Point out each leukocyte.
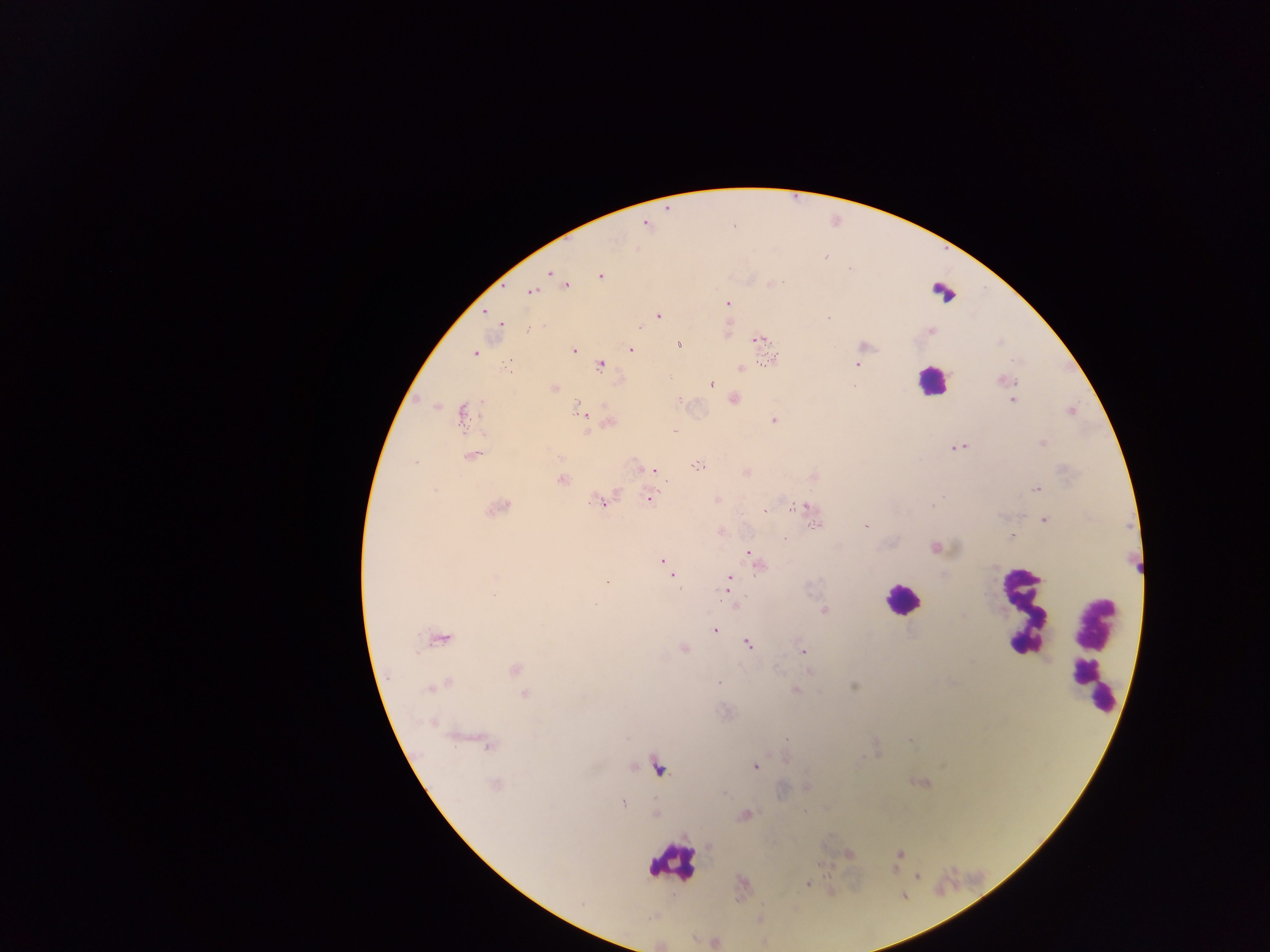

Approximate centers as [x, y] in pixels.
Leukocytes: [943, 293], [932, 380], [901, 598], [1024, 612], [1097, 652], [672, 861].

field of view = single
country = Ghana
image size = 1270×952 pixels
capture = mobile-phone photograph through a microscope
malaria parasite locations = approximate centers as [x, y] in pixels: [666, 209], [646, 225], [551, 272], [600, 276], [771, 284], [566, 285], [532, 291], [728, 303], [484, 311], [658, 316], [500, 324], [639, 328], [931, 330], [757, 340], [679, 343], [864, 345], [630, 349], [574, 351], [474, 353], [772, 359], [509, 360], [600, 364], [856, 364], [740, 368], [1003, 380], [710, 383], [554, 388], [733, 398], [1012, 400], [578, 404], [435, 406], [1070, 410], [581, 412], [462, 413], [773, 420], [609, 422], [587, 430], [674, 431], [1043, 442], [959, 446], [470, 455], [696, 465], [654, 469], [745, 471], [813, 477], [561, 479], [1036, 489], [649, 497], [717, 498], [601, 501], [793, 507], [801, 507], [496, 508], [765, 509], [1044, 520], [815, 525], [866, 526], [720, 532], [1012, 536], [935, 548], [749, 551], [754, 558], [663, 560], [758, 565], [672, 576], [730, 576], [606, 581], [727, 582], [727, 590], [735, 607], [823, 610], [714, 630], [438, 638], [746, 642], [684, 648], [803, 650], [515, 669], [439, 685], [853, 686], [795, 689], [525, 693], [433, 721], [488, 744], [755, 765], [658, 766], [920, 782], [495, 785], [806, 787], [622, 801], [744, 815], [847, 853], [899, 854], [917, 875], [807, 882]
preparation = thick blood film